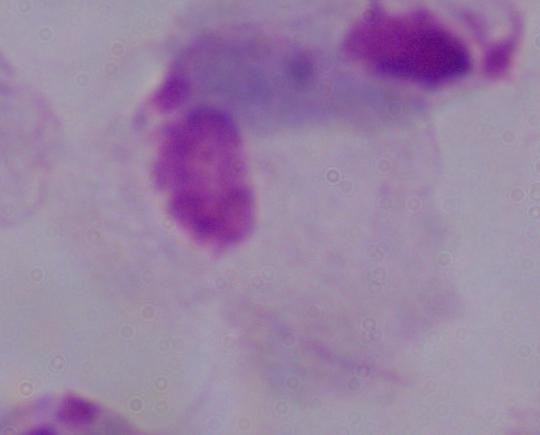

identification = trichomonad
magnification = 1000x
modality = micrograph